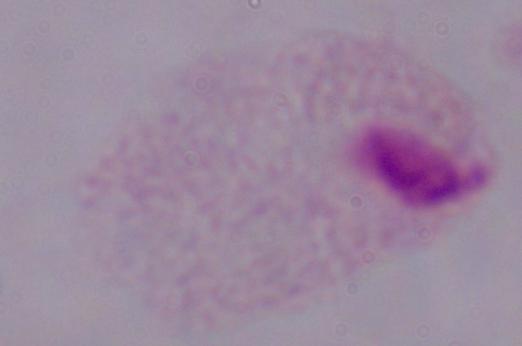
1000x magnification. A trichomonad is seen. Photomicrograph.